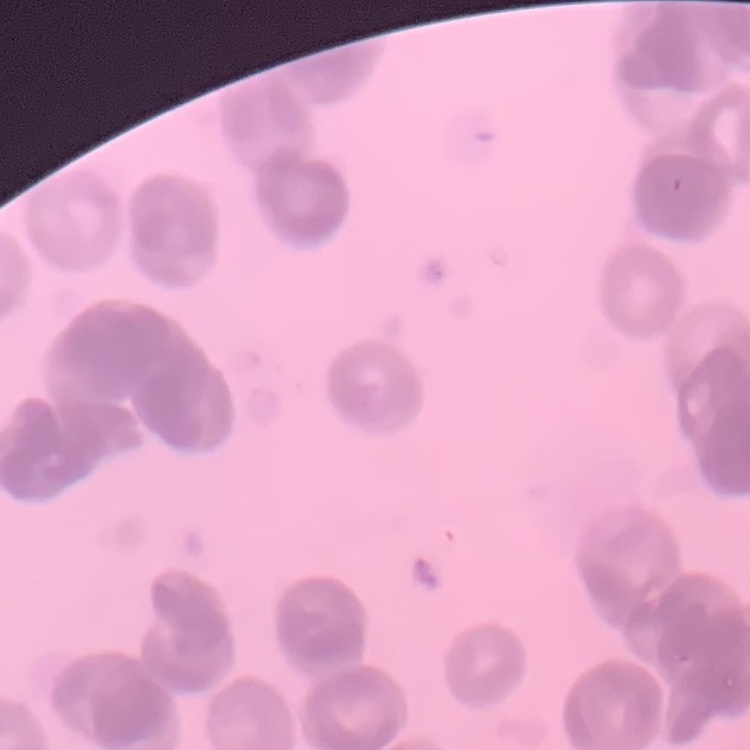
Summary:
  - Red blood cell morphology: rouleaux formation
  - Image type: square crop of a larger photomicrograph
  - Stain: Field's or Giemsa
  - Preparation: thin peripheral smear